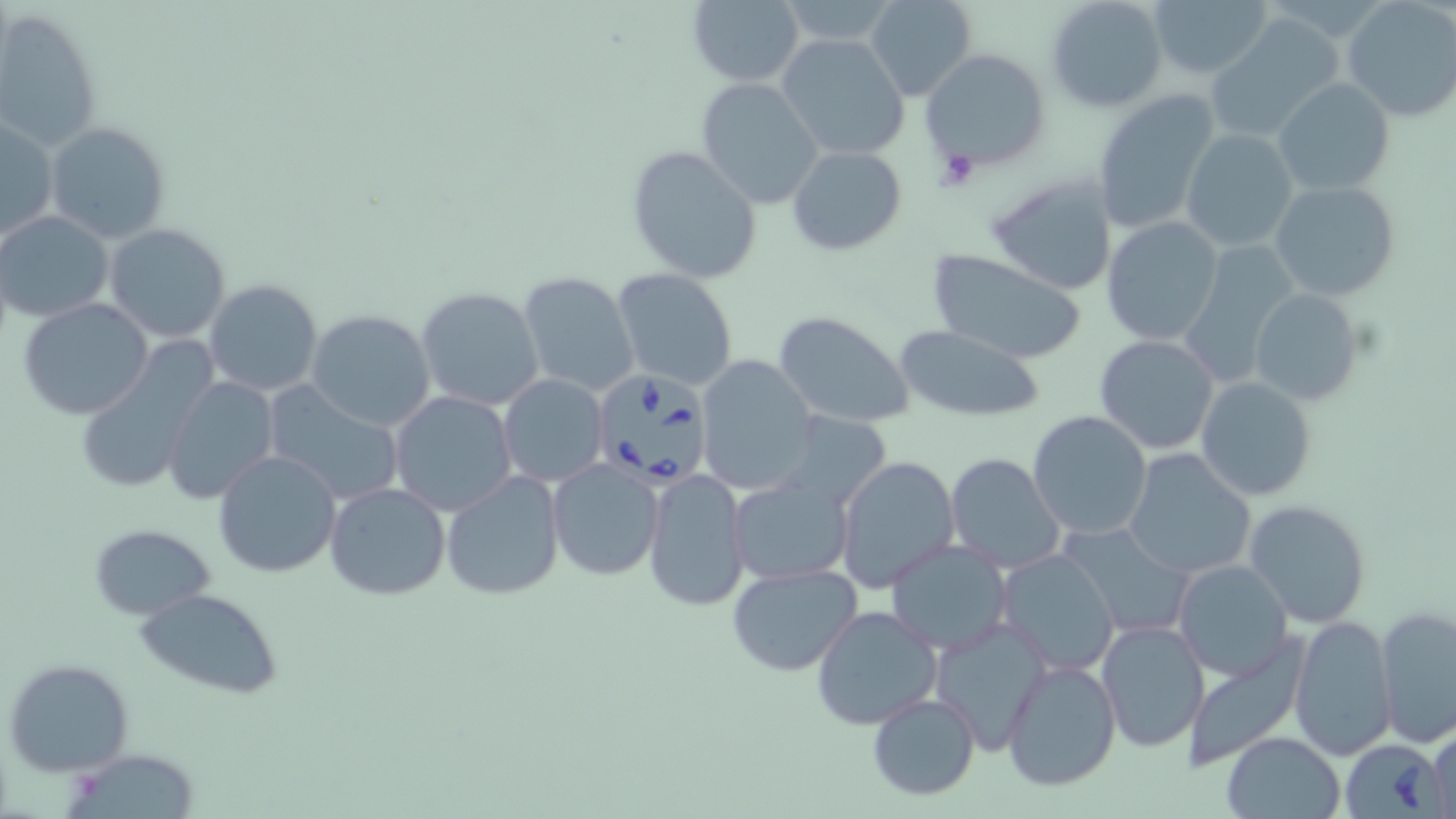
slide-level diagnosis = Babesia divergens
stain = May-Grünwald-Giemsa
modality = optical microscopy
platelet locations = approximate bounding boxes as (x1,y1)-(x2,y2) corner pairs in pixels: (935,149)-(982,190)
image size = 1456×819 pixels
uninfected red blood cell locations = approximate bounding boxes as (x1,y1)-(x2,y2) corner pairs in pixels: (865,0)-(978,101), (1046,0)-(1167,112), (1149,0)-(1271,81), (685,1)-(806,86), (1342,1)-(1456,123), (0,7)-(102,151), (1206,15)-(1343,142), (776,33)-(912,160), (920,49)-(1051,171), (694,78)-(825,210), (1274,78)-(1394,199), (1089,88)-(1222,233), (1,117)-(60,240), (45,122)-(171,245), (1180,128)-(1299,252), (625,145)-(765,284), (787,145)-(907,256), (985,173)-(1117,296), (1269,180)-(1401,303), (1,212)-(113,321), (1101,217)-(1224,346), (104,223)-(232,344), (926,248)-(1088,362), (612,267)-(741,392), (517,271)-(641,397), (204,279)-(325,398), (415,286)-(545,411), (1248,289)-(1361,405), (20,298)-(154,420), (305,308)-(437,430), (772,310)-(918,428), (894,323)-(1047,422), (1094,335)-(1221,455), (71,345)-(215,497), (694,356)-(817,493), (162,375)-(280,505), (498,375)-(608,488), (1196,377)-(1319,501), (261,385)-(403,505), (389,391)-(517,516), (779,411)-(894,512), (1026,411)-(1154,542), (213,448)-(343,578), (1123,449)-(1257,581), (943,453)-(1066,574), (835,455)-(960,594), (547,459)-(663,581), (642,466)-(752,612), (442,471)-(565,598), (727,474)-(854,585), (323,482)-(451,602), (1244,501)-(1371,628), (1060,521)-(1197,640), (87,524)-(215,618), (885,538)-(1013,656), (997,551)-(1120,676), (1172,560)-(1293,680), (726,564)-(862,677), (134,588)-(284,697), (809,604)-(943,731), (1375,606)-(1456,745), (1288,615)-(1398,760), (929,616)-(1052,754), (1095,620)-(1211,753), (1183,641)-(1309,771), (3,657)-(134,776), (1001,659)-(1122,792), (867,692)-(980,801), (1427,721)-(1455,819), (1222,732)-(1347,818), (70,750)-(202,817)
field of view = single
Babesia divergens-infected red blood cell locations = approximate bounding boxes as (x1,y1)-(x2,y2) corner pairs in pixels: (590,368)-(713,487), (1340,739)-(1445,817)
preparation = thin blood film
magnification = 1000x